State the blood parasite species.
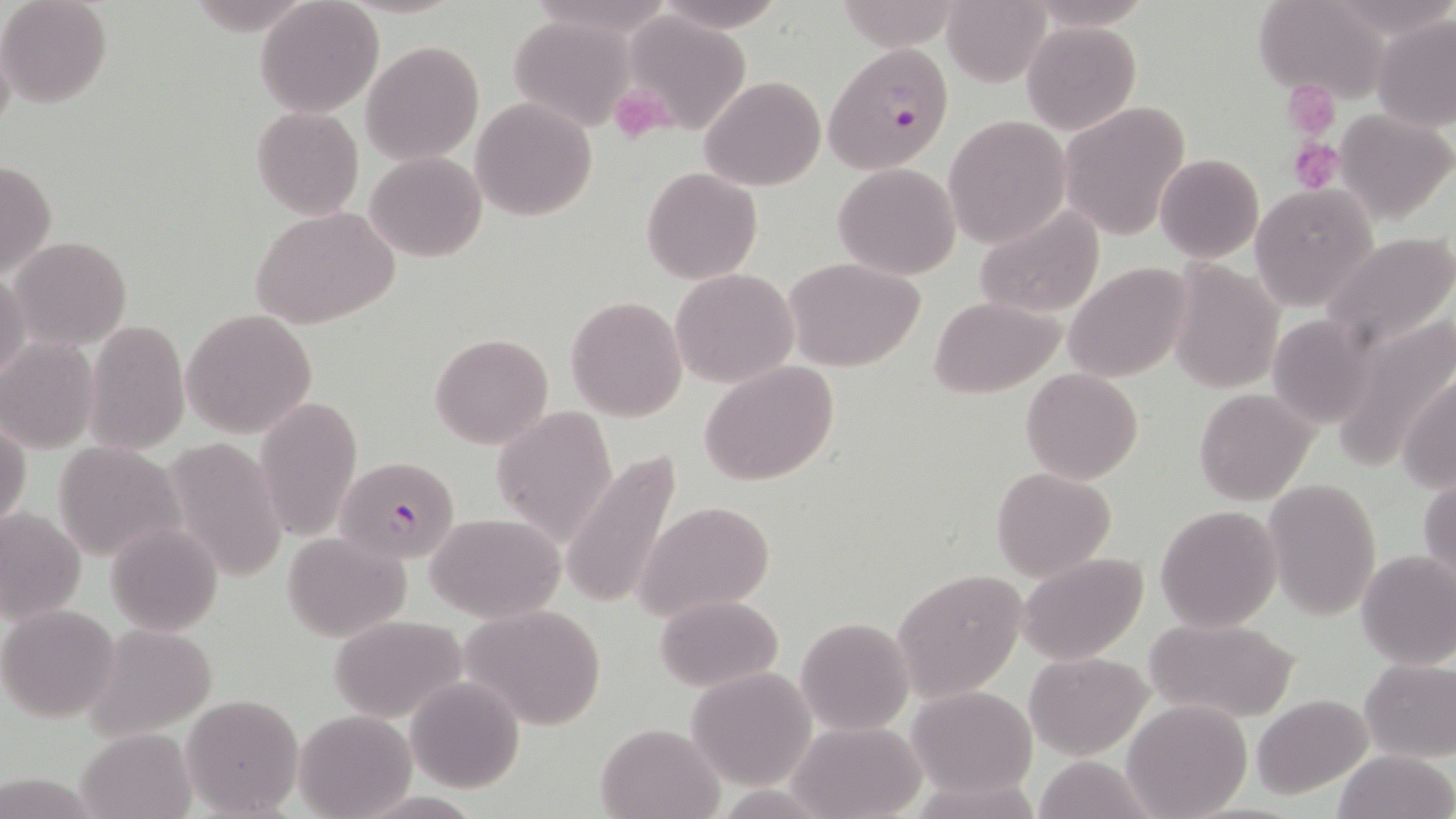
Plasmodium falciparum.

Summary:
  - Coordinate format: approximate bounding boxes as (x1,y1)-(x2,y2) corner pairs in pixels
  - Uninfected red blood cell locations: (1,0)-(112,107), (1254,0)-(1390,102), (254,1)-(383,116), (650,1)-(788,32), (942,1)-(1050,86), (619,9)-(753,135), (1372,13)-(1456,133), (506,16)-(637,129), (1023,22)-(1140,135), (362,40)-(484,165), (699,75)-(826,191), (471,97)-(597,220), (1058,102)-(1189,240), (250,106)-(363,220), (1335,107)-(1455,225), (943,115)-(1070,248), (365,151)-(487,261), (1155,153)-(1264,263), (0,161)-(56,278), (832,164)-(960,280), (642,166)-(762,283), (1249,184)-(1378,309), (251,206)-(401,330), (973,207)-(1106,320), (1319,231)-(1456,355), (9,235)-(131,351), (785,256)-(925,372), (1167,260)-(1283,394), (1064,262)-(1192,383), (0,269)-(29,387), (671,269)-(798,387), (565,296)-(686,422), (930,296)-(1065,398), (181,308)-(317,439), (1268,314)-(1380,428), (1333,319)-(1455,474), (84,320)-(189,454), (429,333)-(553,449), (0,338)-(100,451), (698,362)-(840,485), (1021,368)-(1143,483), (1398,371)-(1456,493), (1194,387)-(1317,504), (254,396)-(363,540), (491,405)-(618,544), (0,417)-(32,532), (164,435)-(287,583), (53,439)-(185,563), (563,450)-(686,610), (991,467)-(1114,580), (1419,472)-(1456,590), (1262,478)-(1381,621), (633,500)-(776,622), (1155,504)-(1284,632), (0,506)-(88,628), (427,512)-(567,623), (106,522)-(222,636), (282,531)-(408,642), (1356,550)-(1456,670), (1018,553)-(1148,664), (892,570)-(1029,701), (652,595)-(781,691), (1,605)-(120,723), (461,605)-(609,730), (328,615)-(466,721), (1146,615)-(1300,722), (796,616)-(914,735), (86,622)-(218,740), (1025,652)-(1150,760), (1359,657)-(1456,761), (687,668)-(817,789), (405,676)-(525,792), (908,687)-(1039,800), (180,692)-(305,818), (1252,694)-(1373,801), (1120,699)-(1252,819), (294,709)-(416,818), (787,720)-(926,819), (595,721)-(725,818), (76,727)-(197,819), (1333,750)-(1454,819), (1034,754)-(1155,819)
  - Platelet locations: (1287,86)-(1339,134), (612,87)-(673,144), (1288,138)-(1342,191)
  - Plasmodium falciparum-infected red blood cell locations: (826,43)-(956,174), (336,455)-(458,563)
  - Image size: 1456×819 pixels
  - Modality: optical microscopy
  - Stain: May-Grünwald-Giemsa
  - Preparation: thin blood film
  - Field of view: single
  - Magnification: 1000x